State which cell type is depicted.
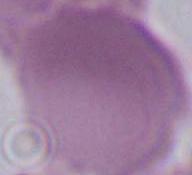

An erythrocyte.

Summary:
  - Magnification: 1000x
  - Modality: micrograph